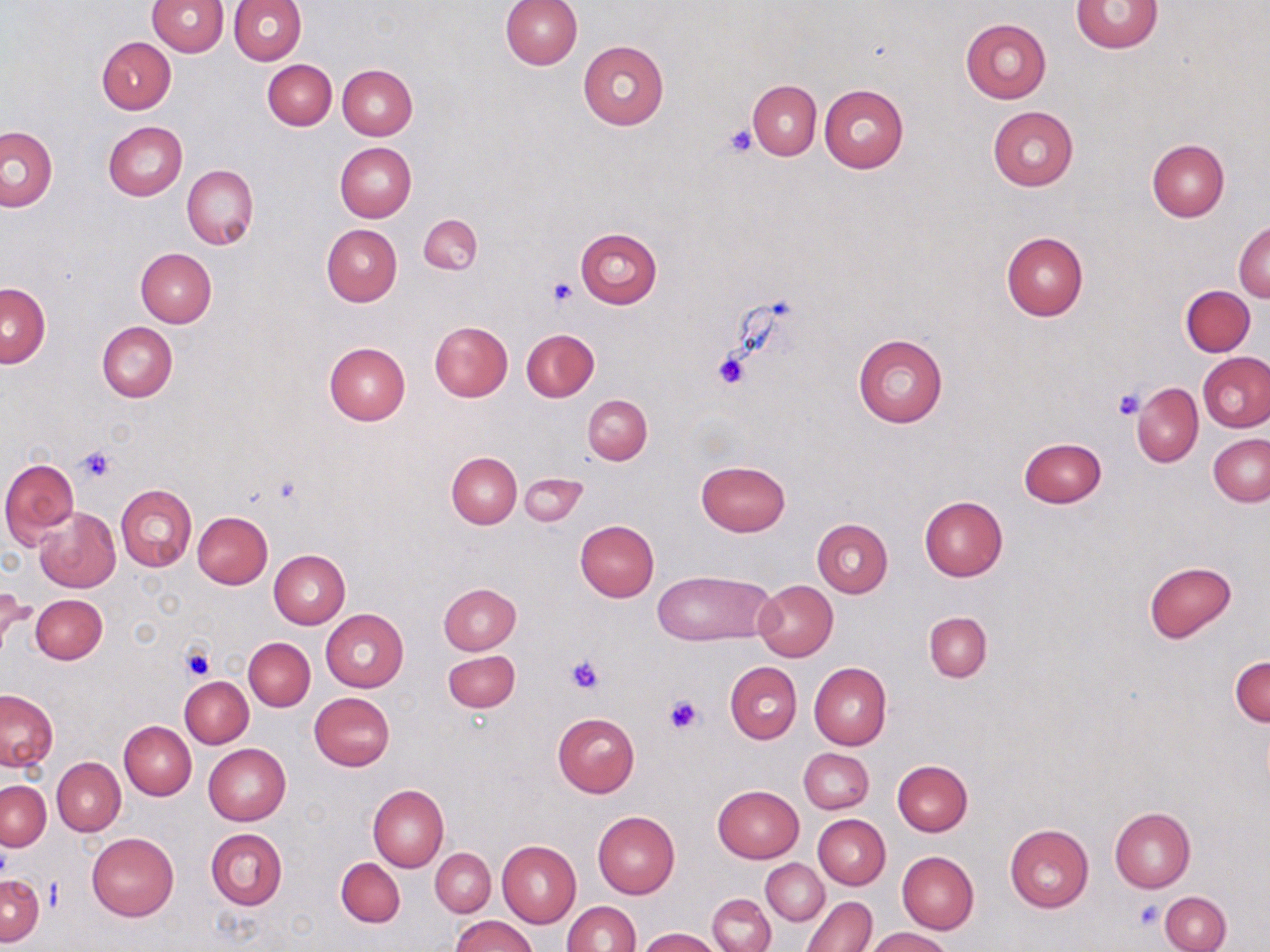 Approximate bounding boxes as (x1, y1, x2, y2) in pixels. Uninfected red blood cell locations: (147, 0, 227, 55), (228, 0, 306, 65), (500, 0, 582, 70), (1071, 1, 1164, 53), (961, 17, 1050, 103), (97, 36, 176, 113), (578, 41, 669, 130), (263, 59, 336, 130), (338, 65, 417, 140), (748, 80, 821, 159), (820, 84, 908, 174), (987, 107, 1078, 191), (103, 121, 188, 199), (1, 126, 57, 211), (1147, 140, 1228, 221), (335, 142, 417, 222), (181, 165, 258, 251), (418, 214, 482, 273), (1233, 221, 1270, 302), (321, 224, 401, 306), (575, 227, 663, 308), (1002, 233, 1088, 320), (136, 248, 217, 326), (1, 283, 50, 366), (1181, 285, 1254, 356), (97, 321, 178, 402), (430, 321, 512, 401), (520, 328, 599, 402), (853, 334, 948, 427), (324, 342, 409, 426), (1198, 351, 1269, 432), (1132, 382, 1203, 467), (583, 394, 652, 465), (1208, 434, 1270, 506), (1019, 437, 1106, 508), (447, 451, 521, 528), (0, 458, 78, 546), (695, 460, 791, 536), (519, 472, 587, 527), (116, 484, 195, 571), (919, 496, 1008, 581), (34, 507, 119, 593), (193, 511, 273, 588), (812, 519, 893, 598), (574, 520, 658, 601), (269, 550, 349, 629), (1144, 561, 1237, 643), (654, 570, 772, 644), (753, 580, 838, 661), (439, 583, 520, 654), (2, 584, 31, 652), (29, 594, 107, 664), (321, 609, 409, 691), (924, 612, 991, 681), (244, 637, 315, 711), (443, 650, 520, 711), (1230, 654, 1269, 727), (809, 661, 892, 750), (726, 662, 802, 744), (181, 675, 253, 747), (0, 690, 57, 771), (310, 692, 394, 771), (552, 712, 639, 796), (119, 720, 195, 799), (204, 743, 291, 825), (808, 745, 879, 888), (799, 748, 873, 814), (52, 758, 125, 836), (893, 759, 972, 836), (1, 780, 50, 851), (368, 784, 448, 873), (713, 785, 804, 862), (1109, 807, 1196, 892), (593, 811, 680, 897), (814, 815, 890, 889), (1005, 824, 1094, 912), (206, 828, 288, 909), (87, 832, 178, 920), (497, 841, 581, 927), (432, 849, 495, 916), (898, 851, 978, 934), (336, 858, 405, 927), (761, 859, 828, 925), (1, 874, 42, 945), (1161, 891, 1231, 952), (707, 894, 775, 952), (801, 896, 877, 952), (562, 901, 640, 952), (452, 915, 536, 952), (636, 927, 722, 951), (866, 927, 953, 952). Platelet locations: (724, 125, 758, 157), (546, 278, 576, 306), (712, 351, 751, 390), (1112, 388, 1146, 420), (75, 445, 118, 483), (182, 644, 214, 680), (563, 655, 606, 695), (663, 693, 704, 734), (1135, 901, 1164, 930). Slide-level diagnosis: negative for blood parasites. 1000x magnification. Thin blood film. One field of a larger specimen. Optical microscopy. May-Grünwald-Giemsa stain. Image is 1270×952 pixels.